Classify this cell by malaria status.
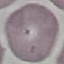

Uninfected.

stain = Giemsa
preparation = thin smear
image type = automatically extracted cell patch, resized to 64 × 64 pixels
capture = smartphone camera at the microscope eyepiece